Give the extent of all Plasmodium vivax-infected red blood cells.
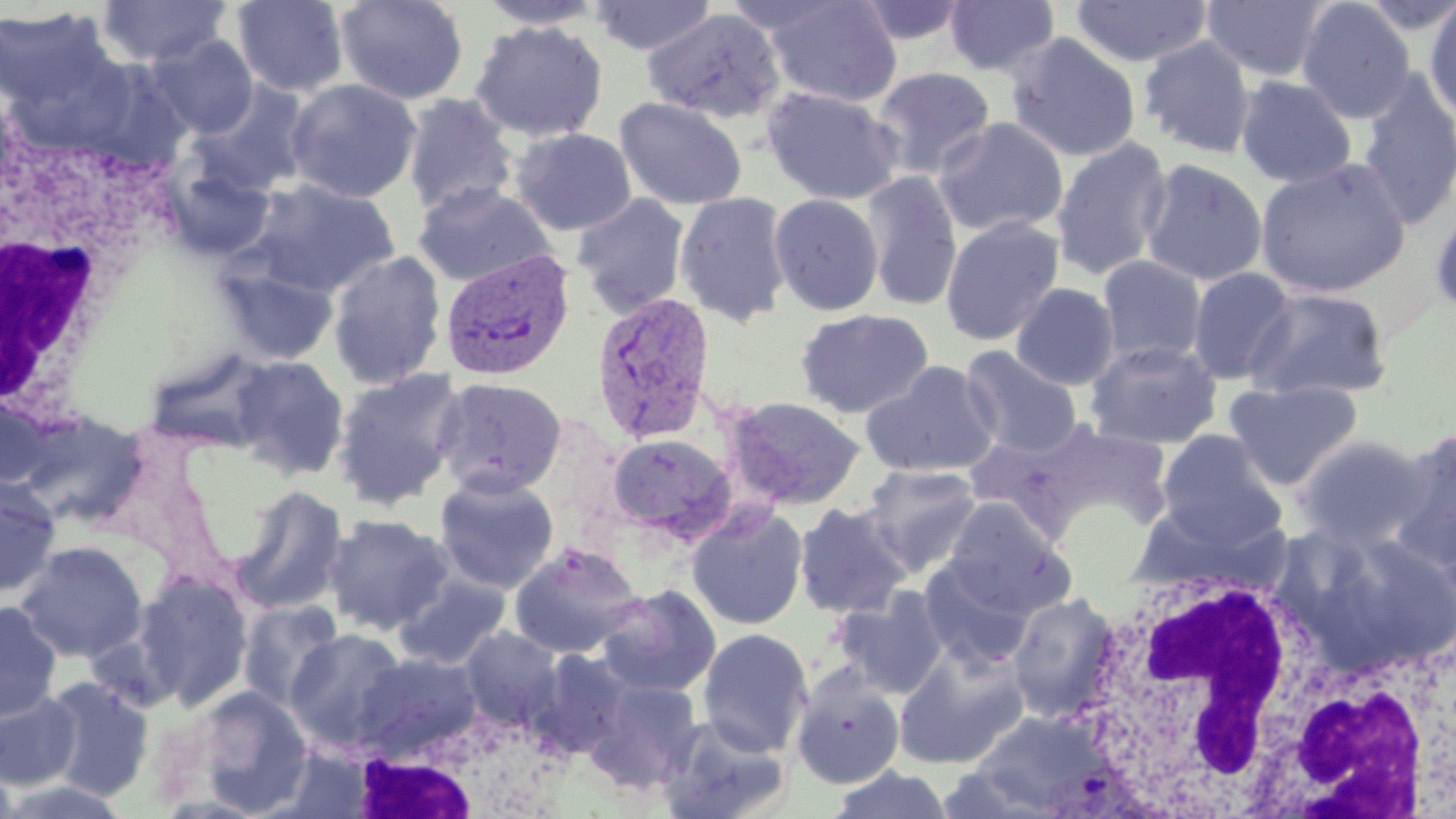
Approximate bounding boxes as [x1, y1, x2, y2] in pixels.
Plasmodium vivax-infected red blood cells: [439, 248, 577, 382], [590, 290, 717, 446].

{
  "slide_level_diagnosis": "Plasmodium vivax",
  "uninfected_red_blood_cell_locations": "approximate bounding boxes as [x1, y1, x2, y2] in pixels: [96, 0, 232, 68], [232, 0, 349, 96], [334, 0, 469, 105], [475, 0, 610, 29], [588, 0, 718, 56], [944, 0, 1060, 78], [1071, 0, 1213, 67], [1200, 0, 1332, 82], [1423, 0, 1456, 123], [761, 1, 903, 108], [852, 1, 971, 46], [1296, 1, 1416, 123], [0, 6, 121, 126], [642, 8, 787, 125], [470, 21, 609, 142], [1006, 32, 1141, 163], [149, 33, 259, 139], [1138, 35, 1256, 159], [871, 66, 997, 180], [1356, 73, 1456, 230], [1235, 75, 1357, 188], [285, 79, 422, 203], [189, 81, 313, 197], [761, 87, 903, 206], [402, 93, 519, 218], [614, 97, 748, 210], [933, 116, 1068, 238], [510, 127, 638, 236], [1050, 137, 1174, 281], [1255, 157, 1411, 298], [158, 158, 277, 261], [1138, 159, 1268, 286], [861, 171, 963, 313], [245, 180, 400, 298], [413, 182, 557, 288], [674, 190, 792, 327], [572, 193, 691, 318], [769, 193, 884, 316], [1429, 200, 1456, 321], [940, 216, 1064, 346], [327, 251, 447, 390], [1097, 255, 1207, 366], [216, 259, 339, 366], [1187, 267, 1298, 385], [1010, 283, 1120, 390], [1244, 287, 1392, 401], [795, 308, 934, 419], [1086, 340, 1223, 450], [960, 345, 1082, 458], [229, 356, 349, 479], [860, 361, 1000, 478], [332, 367, 467, 510], [433, 377, 567, 498], [1224, 379, 1364, 491], [726, 396, 866, 510], [1390, 428, 1456, 565], [1157, 429, 1288, 548], [604, 433, 736, 544], [1295, 435, 1430, 549], [859, 463, 984, 578], [434, 472, 559, 593], [0, 474, 62, 600], [231, 485, 349, 614], [942, 498, 1072, 617], [793, 502, 912, 618], [686, 503, 809, 630], [323, 513, 454, 635], [16, 540, 149, 662], [508, 542, 643, 659], [919, 559, 1034, 670], [393, 572, 512, 670], [130, 573, 254, 708], [594, 583, 722, 699], [831, 585, 951, 699], [1008, 592, 1121, 722], [0, 600, 63, 722], [238, 600, 345, 711], [459, 626, 565, 729], [285, 628, 410, 752], [696, 628, 814, 756], [893, 645, 1030, 770], [529, 648, 637, 758], [354, 651, 483, 759], [789, 666, 906, 790], [583, 676, 704, 795], [41, 677, 155, 800], [188, 687, 314, 814], [0, 689, 82, 790], [656, 715, 792, 819], [0, 757, 22, 819], [828, 766, 955, 819]",
  "white_blood_cell_locations": "approximate bounding boxes as [x1, y1, x2, y2] in pixels: [0, 112, 169, 434], [1069, 553, 1331, 816], [1260, 633, 1456, 819], [344, 702, 564, 819]",
  "image_size": "1456×819 pixels",
  "field_of_view": "single",
  "modality": "optical microscopy",
  "stain": "May-Grünwald-Giemsa",
  "preparation": "thin blood film",
  "magnification": "1000x"
}